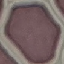

Malaria status: uninfected. Thin smear of blood. Giemsa stain. Cell patch, automatically extracted from a larger field of view and resized to 64 × 64 pixels. Photographed with a smartphone camera at the microscope eyepiece.